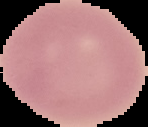
Summary:
  - Image type: segmented cell region on a black background
  - Image size: 148×127 pixels
  - Result: negative for Plasmodium parasites
  - Preparation: thin blood film